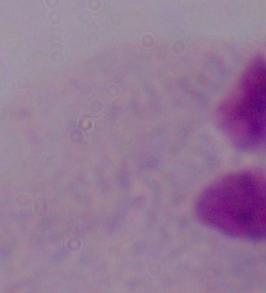
magnification = 1000x
identification = trichomonad
modality = micrograph